Locate every malaria parasite.
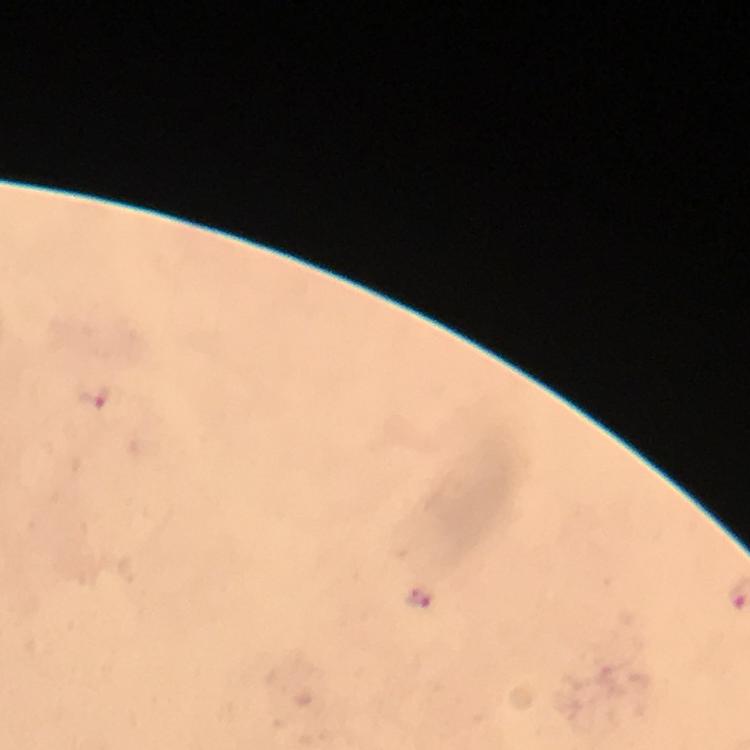

Approximate centers as {x, y} in pixels.
Malaria parasites: {97, 398}, {416, 596}.

Summary:
  - Cropped from: one field of view
  - Context: from a malaria diagnostic workup
  - Stain: Giemsa
  - Image size: 750×750 pixels
  - Capture: smartphone photograph through a microscope
  - Preparation: thick smear
  - Immersion oil: used
  - Magnification: 100x